Classify this cell by malaria status.
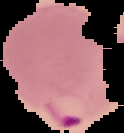
Parasitized.

preparation = thin blood film
image type = segmented cell region with the area outside set to black
image size = 124×133 pixels